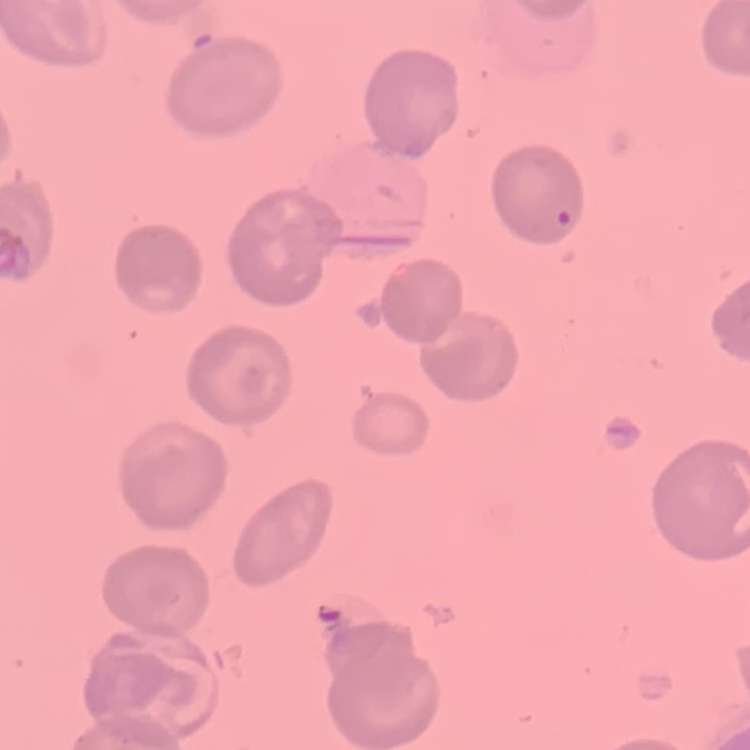 The red blood cells exhibit no rouleaux formation. Field's or Giemsa stain. Square crop of a larger photomicrograph. Thin peripheral smear.